State which parasite is depicted.
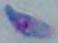

This is Toxoplasma gondii.

Summary:
  - Modality: photomicrograph
  - Magnification: 1000x